Name the parasite shown.
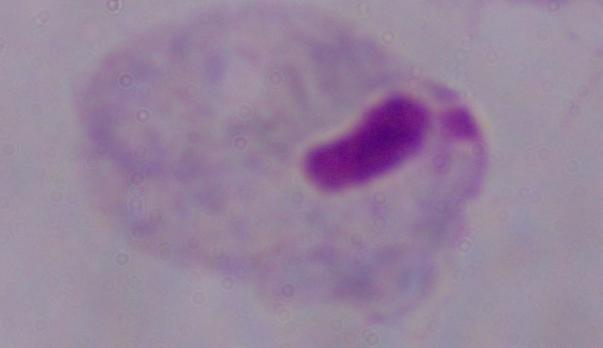
A trichomonad.

Summary:
  - Modality: micrograph
  - Magnification: 1000x